Identify the cell.
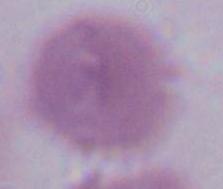

An erythrocyte.

magnification: 1000x
modality: micrograph